Identify the cell.
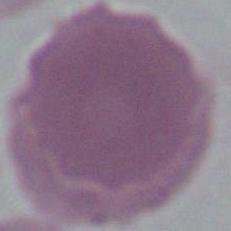

An erythrocyte.

Summary:
  - Magnification: 1000x
  - Modality: photomicrograph